Report the malaria status of this cell.
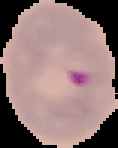
Parasitized.

Summary:
  - Preparation: thin blood smear
  - Image size: 118×148 pixels
  - Image type: segmented cell region with the area outside set to black